Describe the morphology of the erythrocytes.
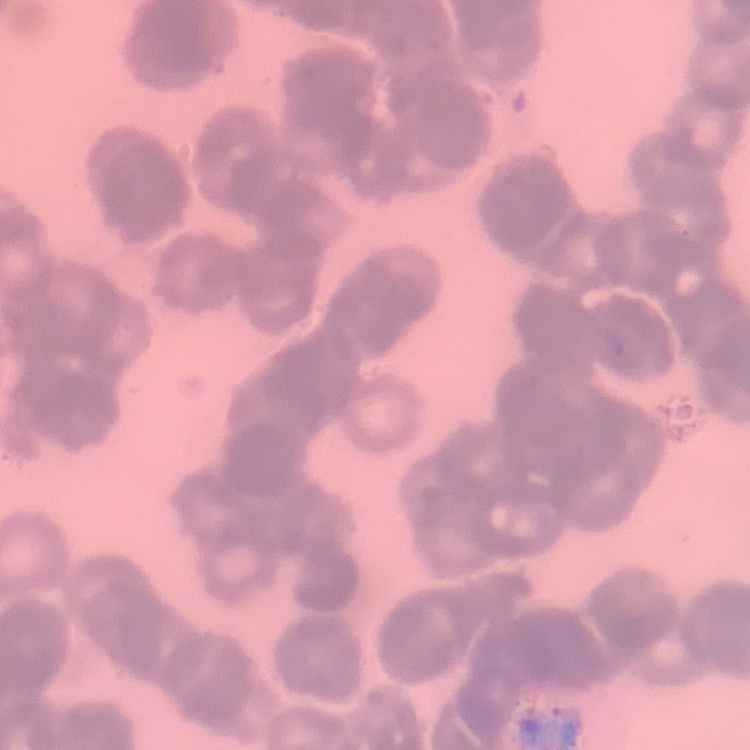
Rouleaux formation.

{
  "image_type": "one tile cut from a larger photomicrograph",
  "stain": "Field's or Giemsa",
  "preparation": "thin blood smear"
}